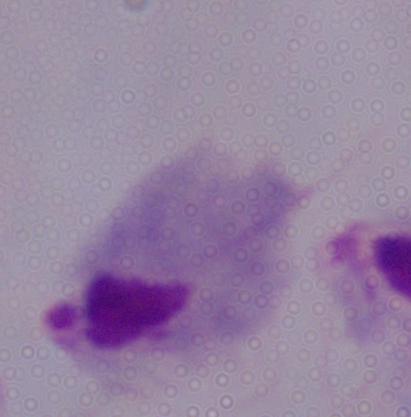
Summary:
  - Modality: photomicrograph
  - Identification: trichomonad
  - Magnification: 1000x